State which parasite is depicted.
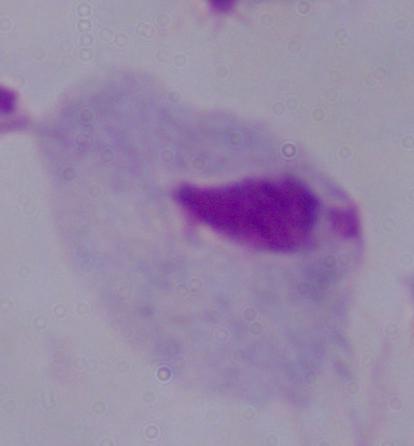

A trichomonad.

magnification = 1000x
modality = micrograph